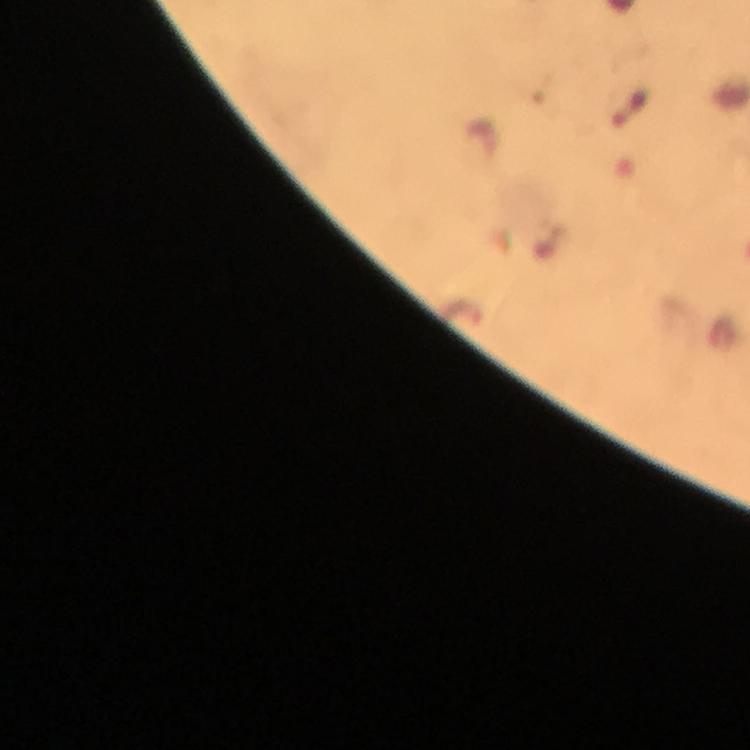

Approximate centers as (x, y) in pixels.
Summary:
  - Plasmodium parasite locations: (631, 105)
  - Context: from a malaria diagnostic workup
  - Immersion oil: used
  - Preparation: thick smear
  - Capture: smartphone mounted on the microscope
  - Magnification: 100x
  - Image size: 750×750 pixels
  - Cropped from: a single field of view
  - Stain: Giemsa